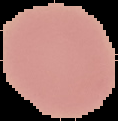
Cell region segmented out of the field of view; the surrounding area is masked to black. Image is 118×121 pixels. Result: no malaria parasites detected. From a thin blood smear.